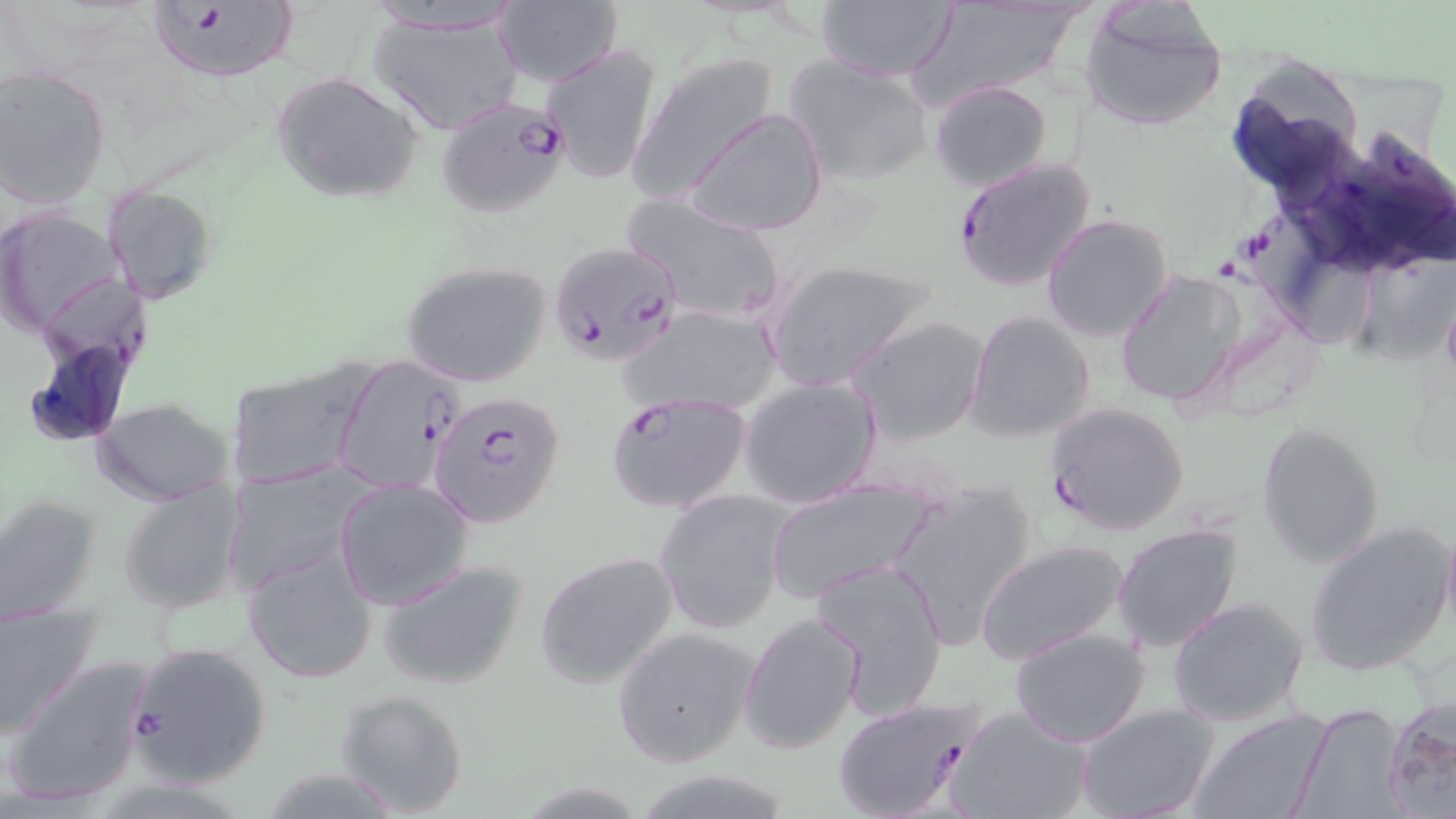

slide_level_diagnosis: Plasmodium falciparum
field_of_view: single
uninfected_red_blood_cell_locations: 'approximate bounding boxes as (x1,y1)-(x2,y2) corner pairs in pixels: (912,0)-(1087,107), (494,2)-(624,86), (814,2)-(957,81), (1079,5)-(1227,131), (368,7)-(526,136), (539,42)-(664,185), (628,54)-(781,205), (786,55)-(933,183), (0,66)-(111,208), (270,70)-(424,203), (929,80)-(1054,193), (683,108)-(827,237), (105,185)-(218,305), (622,193)-(789,328), (0,207)-(123,336), (1042,213)-(1172,343), (763,258)-(931,393), (401,259)-(555,391), (1112,270)-(1247,408), (624,304)-(782,418), (965,310)-(1095,442), (848,315)-(991,447), (330,353)-(461,498), (224,361)-(373,489), (738,375)-(883,507), (94,398)-(234,506), (1257,420)-(1386,568), (224,464)-(368,595), (116,477)-(244,615), (333,478)-(475,611), (765,479)-(939,602), (886,482)-(1035,647), (655,490)-(791,635), (0,494)-(100,623), (1440,518)-(1456,642), (1111,522)-(1244,651), (1304,522)-(1455,675), (975,539)-(1130,664), (241,542)-(380,682), (533,550)-(681,689), (810,557)-(950,717), (376,558)-(530,691), (1168,597)-(1309,726), (0,600)-(101,740), (738,610)-(866,756), (611,626)-(760,767), (1008,626)-(1152,748), (4,653)-(158,810), (333,689)-(470,817), (1383,699)-(1456,818), (1076,703)-(1219,819), (1290,703)-(1411,819), (946,705)-(1094,819), (1191,710)-(1331,819), (635,771)-(797,819)'
stain: May-Grünwald-Giemsa
preparation: thin blood smear
image_size: 1456×819 pixels
plasmodium_falciparum_infected_red_blood_cell_locations: 'approximate bounding boxes as (x1,y1)-(x2,y2) corner pairs in pixels: (145,0)-(303,84), (435,97)-(573,217), (951,155)-(1097,292), (546,241)-(683,368), (606,390)-(754,514), (430,393)-(566,528), (1045,401)-(1191,536), (123,640)-(273,787), (832,697)-(984,819)'
magnification: 1000x
modality: optical microscopy